Locate and identify every blood parasite.
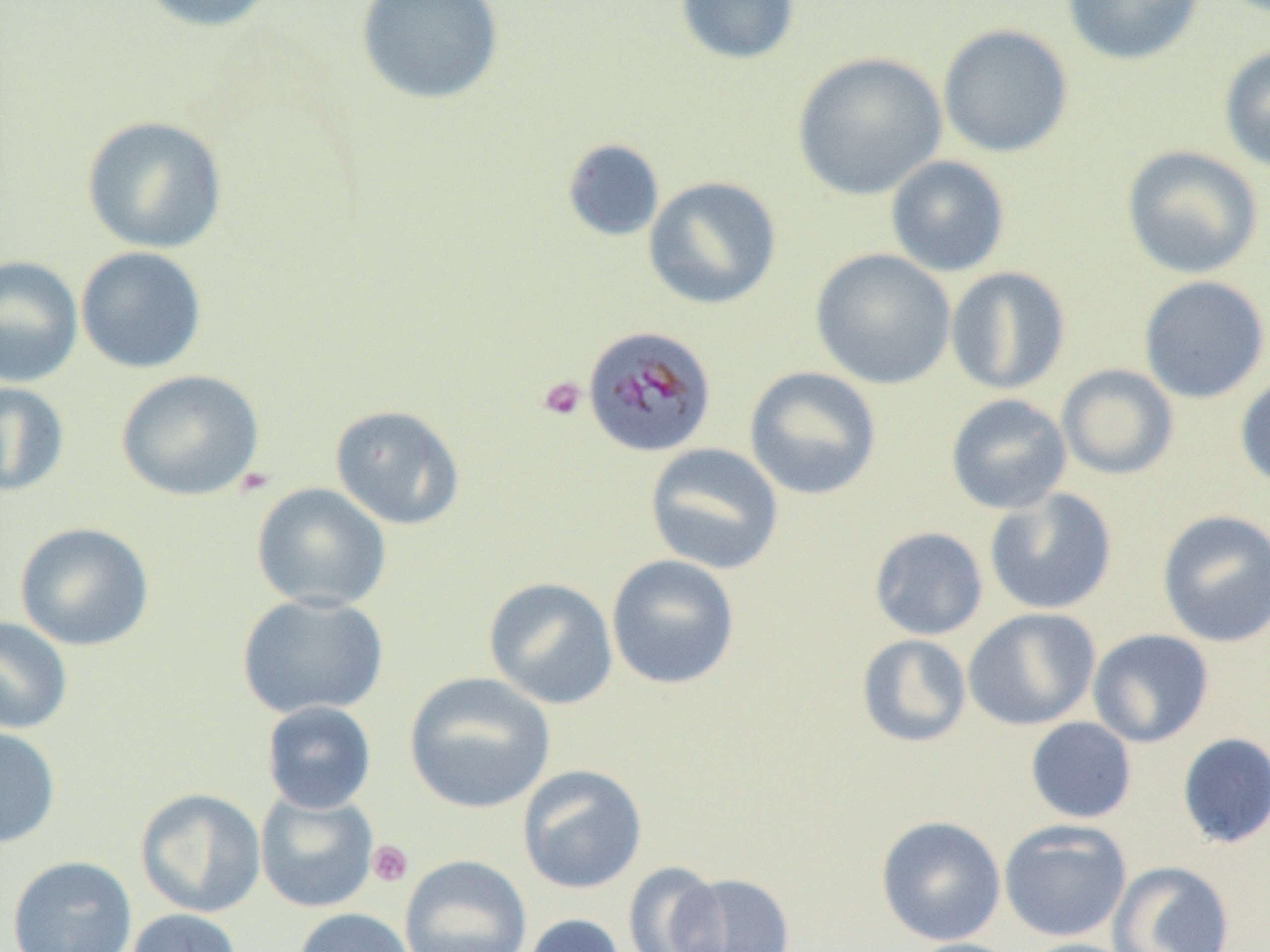

Approximate bounding boxes as [x1, y1, x2, y2] in pixels.
Plasmodium malariae-infected red blood cells: [582, 325, 717, 458].
No Plasmodium falciparum, Plasmodium ovale, Plasmodium vivax, Babesia divergens, or Trypanosoma brucei observed.

slide_level_diagnosis: Plasmodium malariae
preparation: thin blood smear
image_size: 1270×952 pixels
platelet_locations: 'approximate bounding boxes as [x1, y1, x2, y2] in pixels: [537, 376, 587, 421], [367, 840, 413, 887]'
uninfected_red_blood_cell_locations: 'approximate bounding boxes as [x1, y1, x2, y2] in pixels: [134, 0, 281, 34], [355, 0, 505, 106], [675, 0, 800, 65], [1062, 0, 1205, 66], [937, 24, 1073, 158], [1218, 45, 1270, 174], [792, 52, 947, 201], [81, 115, 228, 254], [562, 139, 665, 242], [1121, 145, 1264, 279], [885, 155, 1010, 277], [643, 176, 782, 310], [75, 246, 207, 374], [810, 248, 956, 390], [0, 256, 83, 387], [945, 266, 1071, 395], [1138, 275, 1270, 404], [1057, 364, 1179, 481], [744, 366, 882, 500], [115, 369, 265, 501], [1235, 371, 1270, 491], [0, 381, 70, 497], [945, 394, 1072, 515], [330, 404, 466, 531], [644, 443, 784, 574], [251, 483, 393, 612], [984, 488, 1117, 615], [1157, 509, 1270, 647], [15, 522, 154, 652], [868, 526, 988, 640], [606, 554, 740, 690], [483, 577, 618, 709], [237, 593, 389, 719], [963, 608, 1100, 730], [0, 616, 73, 734], [1088, 629, 1214, 748], [856, 633, 972, 747], [404, 671, 556, 814], [261, 701, 377, 814], [1025, 717, 1137, 824], [0, 725, 61, 849], [1177, 732, 1270, 849], [517, 764, 647, 895], [135, 787, 266, 918], [254, 790, 380, 913], [875, 815, 1006, 946], [999, 819, 1132, 942], [7, 855, 137, 951], [399, 855, 531, 952], [1108, 860, 1236, 952], [622, 861, 729, 952], [670, 871, 795, 952], [292, 907, 417, 952], [125, 908, 245, 952], [521, 913, 627, 952], [900, 937, 1029, 952], [1017, 938, 1139, 952]'
magnification: 1000x
modality: light microscopy
field_of_view: one of a larger specimen